Describe the morphology of the red blood cells.
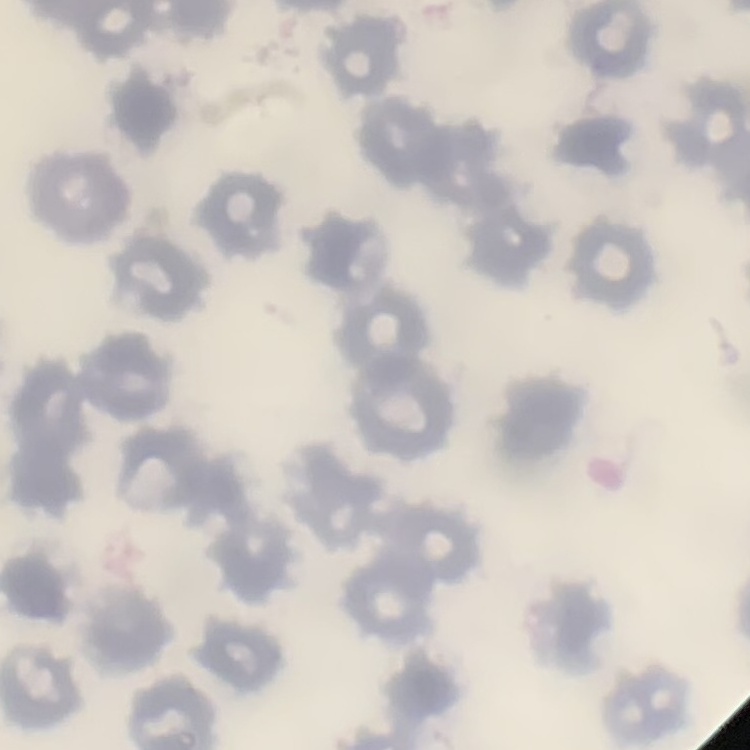

They show no rouleaux formation.

Summary:
  - Preparation: thin peripheral smear
  - Stain: Field's or Giemsa
  - Image type: square crop of a larger photomicrograph